Assess this cell for malaria.
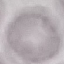
It is uninfected.

stain = Giemsa
capture = smartphone camera at the microscope eyepiece
preparation = thin blood smear
image type = automatically extracted cell patch, resized to 64 × 64 pixels